Assess the morphology of the erythrocytes.
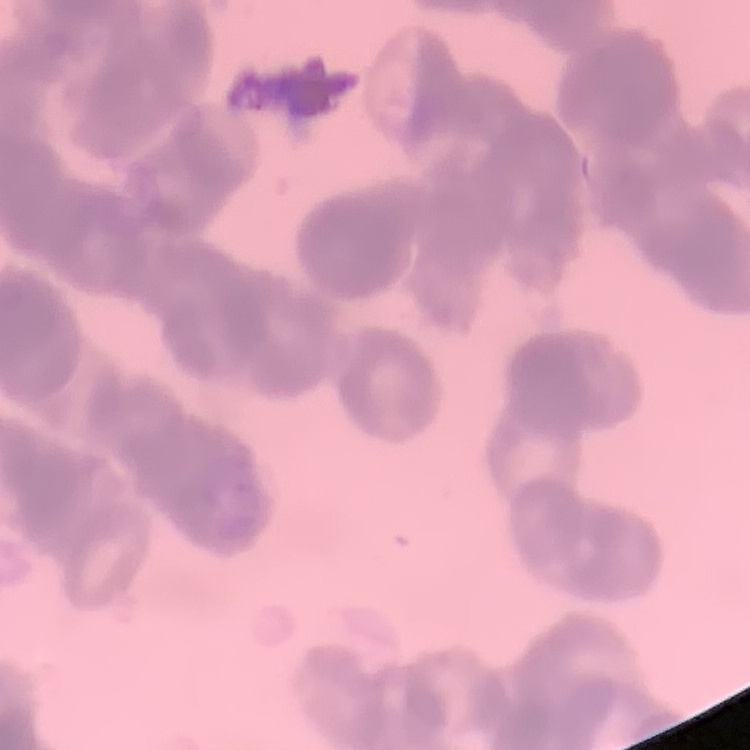

They show rouleaux formation.

Thin peripheral smear. Square crop of a larger photomicrograph. Field's or Giemsa stain.